Comment on the morphology of the red blood cells.
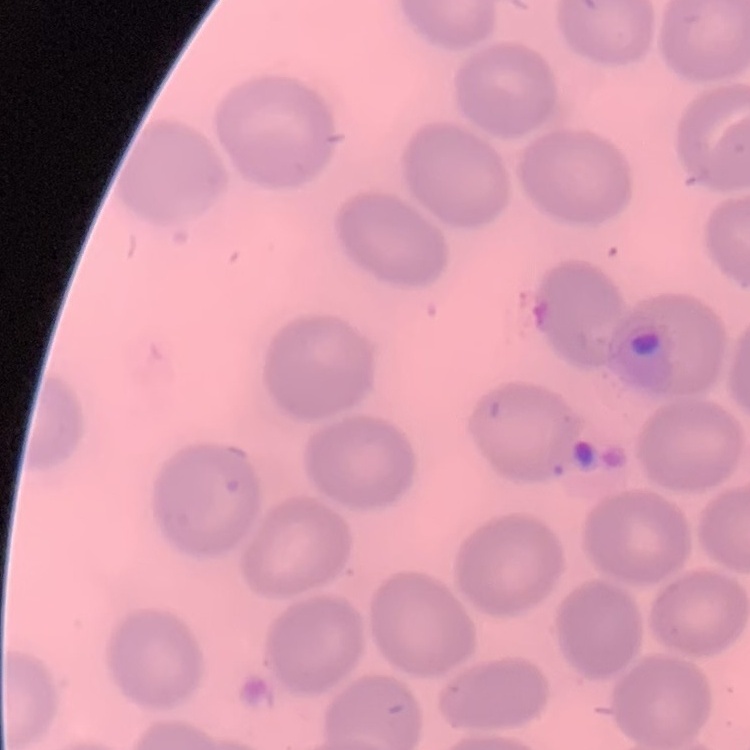

They show no rouleaux formation.

stain = Field's or Giemsa
image type = square crop of a larger photomicrograph
preparation = thin peripheral smear